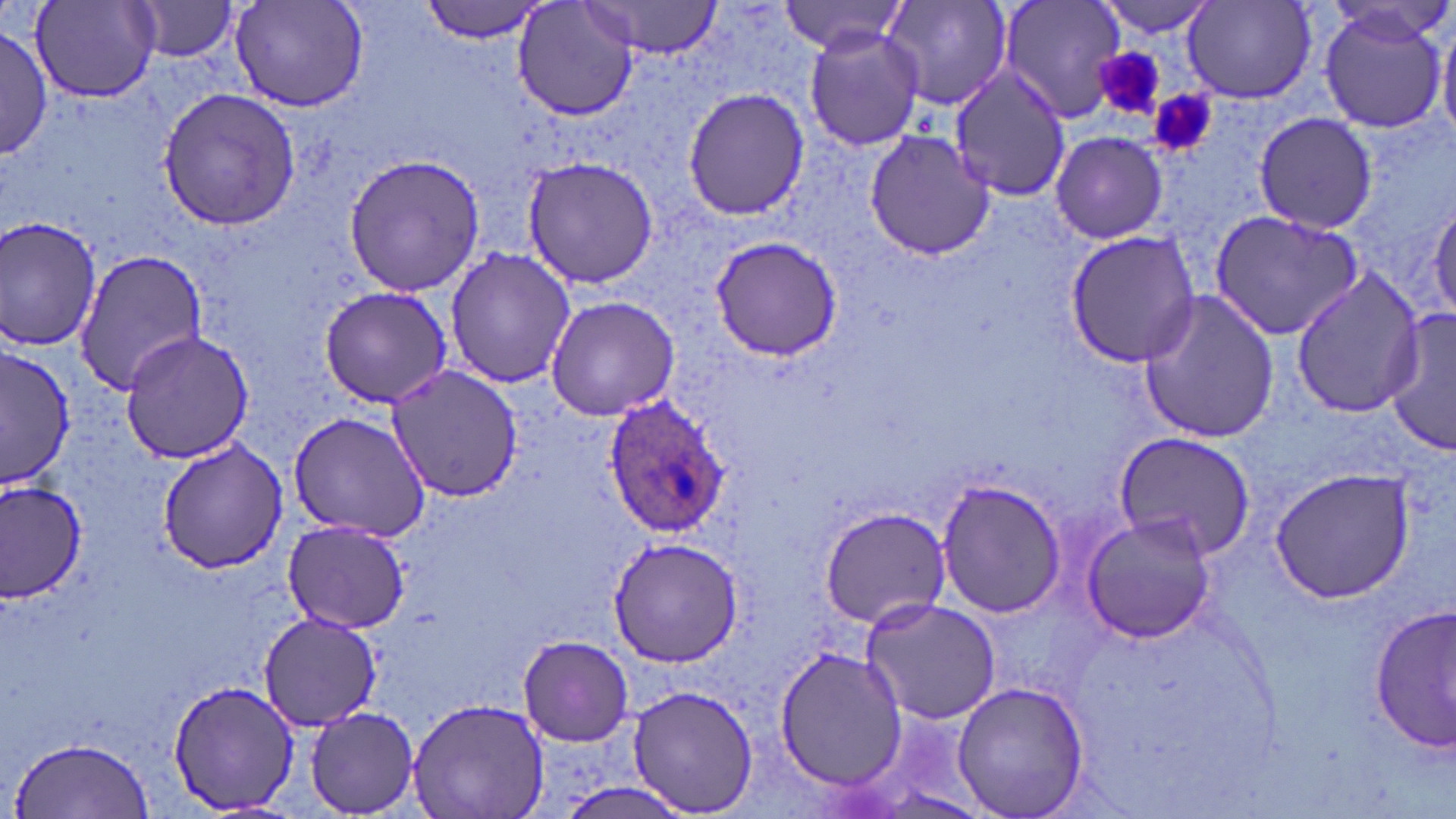

{
  "slide_level_diagnosis": "Plasmodium ovale",
  "uninfected_red_blood_cell_locations": "approximate bounding boxes as (x1,y1)-(x2,y2) corner pairs in pixels: (229,0)-(369,113), (421,0)-(549,42), (514,0)-(640,122), (879,0)-(1013,113), (997,0)-(1127,121), (1092,0)-(1220,36), (30,1)-(162,102), (130,1)-(239,63), (782,1)-(910,56), (582,2)-(724,58), (1182,2)-(1318,104), (1316,3)-(1451,135), (1437,19)-(1456,152), (804,25)-(923,153), (0,28)-(51,161), (948,66)-(1071,200), (157,88)-(301,232), (682,89)-(809,220), (1253,113)-(1379,234), (863,130)-(994,261), (1050,131)-(1169,242), (343,153)-(486,296), (522,156)-(663,288), (1429,194)-(1456,323), (1210,208)-(1364,341), (0,215)-(103,355), (1066,231)-(1202,368), (708,235)-(844,360), (445,246)-(576,389), (74,247)-(206,396), (1288,268)-(1425,418), (318,285)-(454,408), (1140,287)-(1282,444), (545,294)-(679,421), (1386,306)-(1456,459), (120,330)-(255,465), (0,347)-(75,491), (385,364)-(522,504), (285,411)-(431,542), (1111,433)-(1254,558), (156,441)-(291,573), (1267,467)-(1417,604), (2,476)-(85,602), (936,477)-(1067,619), (816,505)-(952,629), (1080,513)-(1218,644), (283,519)-(409,634), (606,537)-(746,666), (858,597)-(1003,725), (1371,605)-(1455,754), (258,612)-(381,731), (519,634)-(633,746), (774,644)-(909,791), (165,678)-(300,815), (950,680)-(1091,819), (626,685)-(762,816), (404,697)-(551,819), (304,706)-(423,816), (11,735)-(154,817)",
  "plasmodium_ovale_infected_red_blood_cell_locations": "approximate bounding boxes as (x1,y1)-(x2,y2) corner pairs in pixels: (602,396)-(731,540)",
  "modality": "light microscopy",
  "magnification": "1000x",
  "field_of_view": "single",
  "stain": "May-Grünwald-Giemsa",
  "image_size": "1456×819 pixels",
  "platelet_locations": "approximate bounding boxes as (x1,y1)-(x2,y2) corner pairs in pixels: (1095,47)-(1163,118), (1152,93)-(1216,158)",
  "preparation": "thin blood film"
}